Mark where leukocytes are.
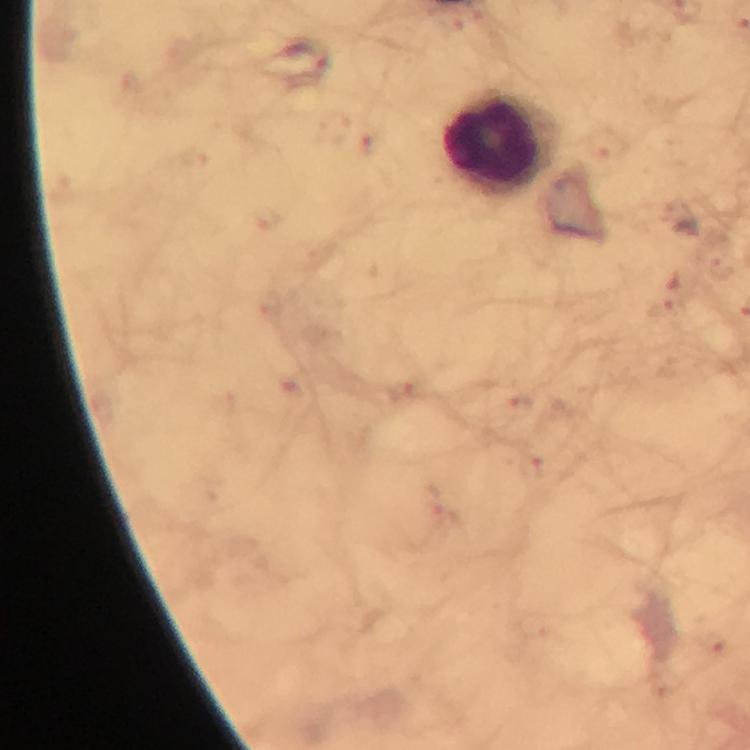
Approximate centers as (x, y) in pixels.
Leukocytes: (499, 144).

Plasmodium parasite locations: (668, 308), (406, 389), (516, 406), (533, 469), (712, 643). Photographed through the microscope with a smartphone camera. Immersion oil applied. At 100x magnification. From a malaria diagnostic workup. Giemsa stain. Thick smear. Image is 750×750 pixels. Cropped region of a single field of view.